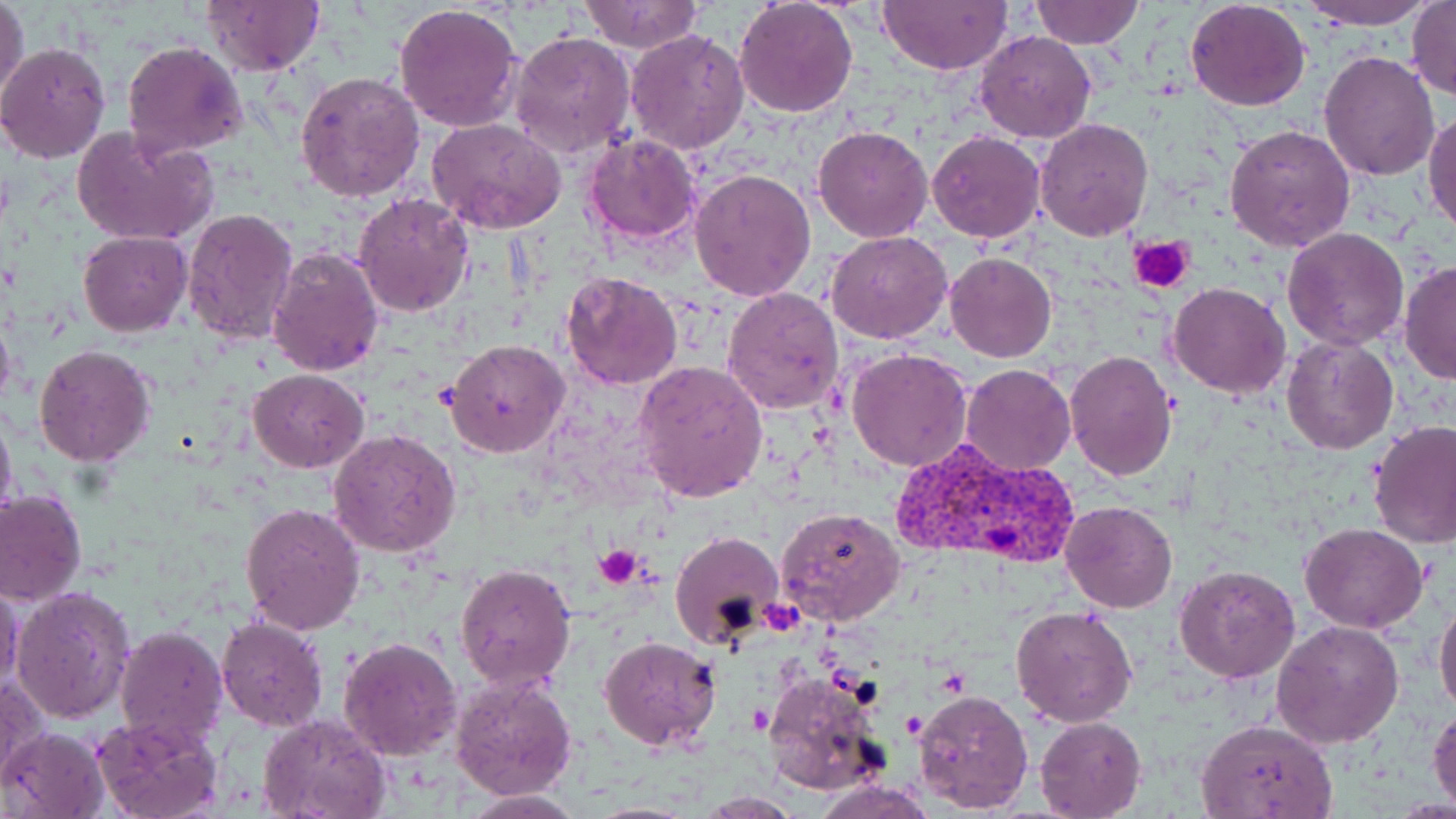 Approximate bounding boxes as (x1, y1, x2, y2) in pixels. Plasmodium vivax-infected red blood cell locations: (893, 438, 1077, 568). Platelet locations: (1131, 236, 1196, 293), (593, 545, 646, 587). Uninfected red blood cell locations: (0, 0, 29, 104), (576, 0, 705, 52), (732, 0, 859, 118), (1031, 0, 1143, 48), (1297, 0, 1440, 28), (200, 1, 326, 75), (878, 1, 1011, 74), (1406, 1, 1454, 103), (1185, 2, 1311, 112), (394, 3, 524, 133), (625, 29, 750, 155), (509, 31, 634, 157), (974, 31, 1097, 143), (122, 39, 250, 156), (0, 43, 109, 163), (1318, 49, 1440, 180), (296, 69, 427, 204), (1423, 107, 1456, 237), (1035, 117, 1153, 241), (425, 118, 568, 236), (72, 123, 218, 248), (1224, 123, 1355, 250), (812, 127, 933, 243), (928, 131, 1046, 243), (580, 134, 701, 244), (689, 167, 817, 303), (353, 191, 474, 319), (183, 208, 299, 345), (1282, 227, 1410, 350), (78, 230, 192, 336), (826, 231, 952, 344), (266, 244, 383, 377), (945, 251, 1057, 363), (1399, 262, 1456, 383), (562, 270, 683, 390), (1168, 283, 1291, 400), (721, 286, 846, 416), (0, 303, 17, 417), (1282, 336, 1398, 454), (445, 339, 568, 458), (33, 344, 156, 466), (848, 346, 971, 470), (1063, 351, 1178, 480), (634, 360, 769, 505), (960, 365, 1075, 477), (248, 368, 368, 473), (0, 407, 17, 524), (1368, 423, 1456, 551), (327, 429, 462, 558), (0, 489, 86, 607), (1061, 502, 1178, 614), (240, 503, 364, 634), (778, 506, 906, 626), (1300, 523, 1428, 633), (668, 529, 786, 651), (456, 561, 577, 691), (1173, 565, 1300, 683), (0, 583, 24, 694), (11, 584, 135, 726), (1434, 595, 1456, 720), (1011, 605, 1138, 728), (216, 617, 329, 732), (1271, 620, 1405, 749), (116, 625, 229, 748), (598, 634, 722, 751), (339, 636, 463, 759), (449, 668, 579, 799), (762, 671, 888, 797), (1, 672, 46, 791), (912, 686, 1033, 813), (1429, 705, 1456, 812), (256, 713, 390, 819), (92, 715, 223, 818), (1035, 716, 1145, 818), (1195, 719, 1338, 818), (3, 725, 107, 819), (813, 777, 938, 819), (460, 791, 584, 817), (698, 793, 806, 817). Slide-level diagnosis: Plasmodium vivax. Captured at 1000x magnification. May-Grünwald-Giemsa stain. Image is 1456×819 pixels. Single field of view. Light microscopy. Thin blood film.